Identify the cell.
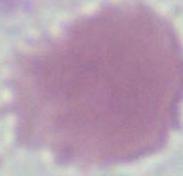

An erythrocyte.

Summary:
  - Magnification: 1000x
  - Modality: photomicrograph